Assess this cell for malaria.
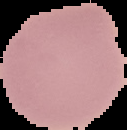

It is uninfected.

Image is 127×130 pixels. Segmented cell region on a black background. From a thin blood film.